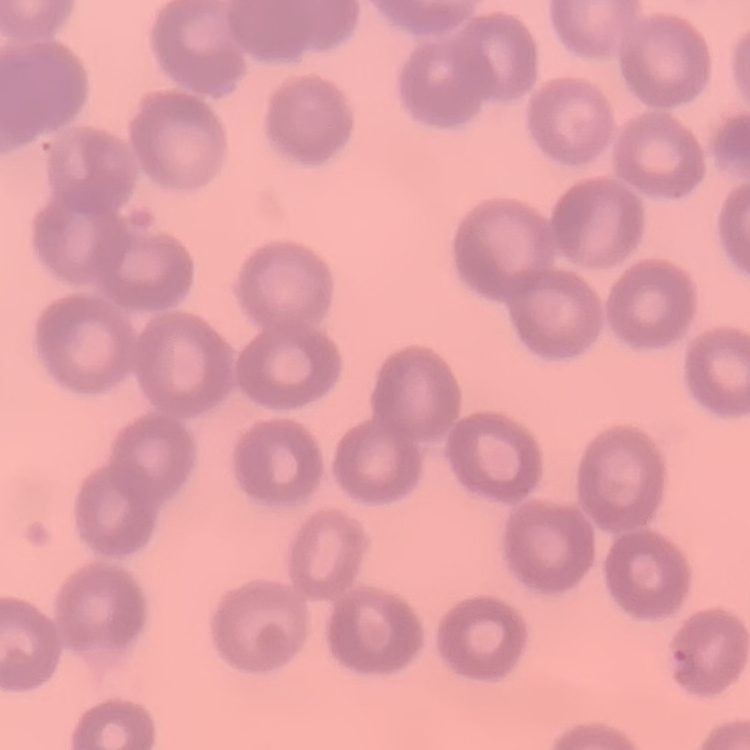 The erythrocytes show no rouleaux formation. Field's or Giemsa stain. Thin blood film. Square crop of a larger photomicrograph.